Comment on the morphology of the erythrocytes.
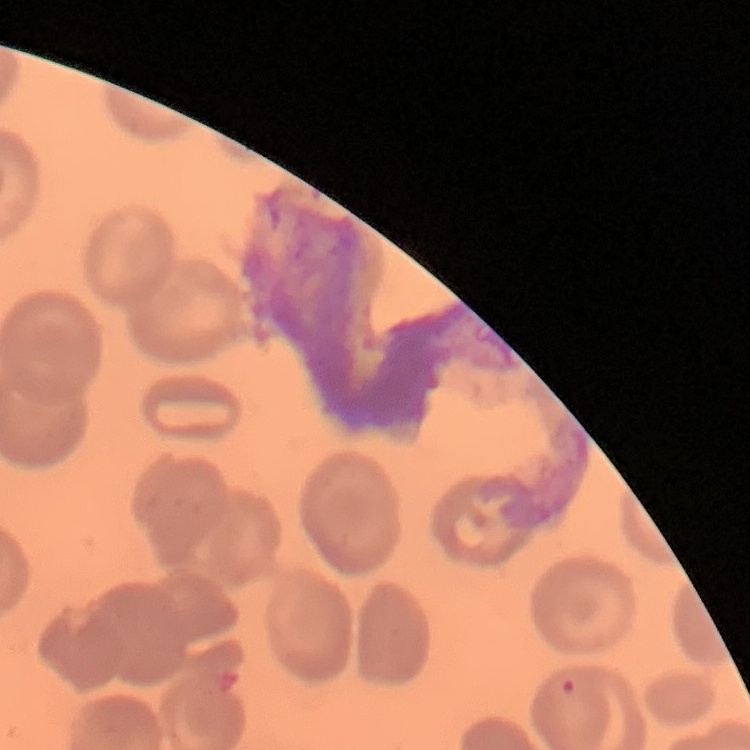
They show no rouleaux formation.

{
  "preparation": "thin blood film",
  "image_type": "square crop of a larger photomicrograph",
  "stain": "Field's or Giemsa"
}